Classify this cell by malaria status.
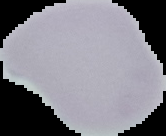
It is uninfected.

From a thin blood film. Image is 166×136 pixels. The area outside the segmented cell region is set to black.